Assess this cell for malaria.
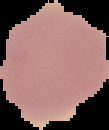
Uninfected.

Summary:
  - Image size: 109×130 pixels
  - Preparation: thin blood smear
  - Image type: segmented cell region on a black background